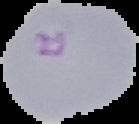
Image is 139×124 pixels. From a thin blood film. Result: malaria parasites detected. Cell region segmented out of the field of view; the surrounding area is masked to black.